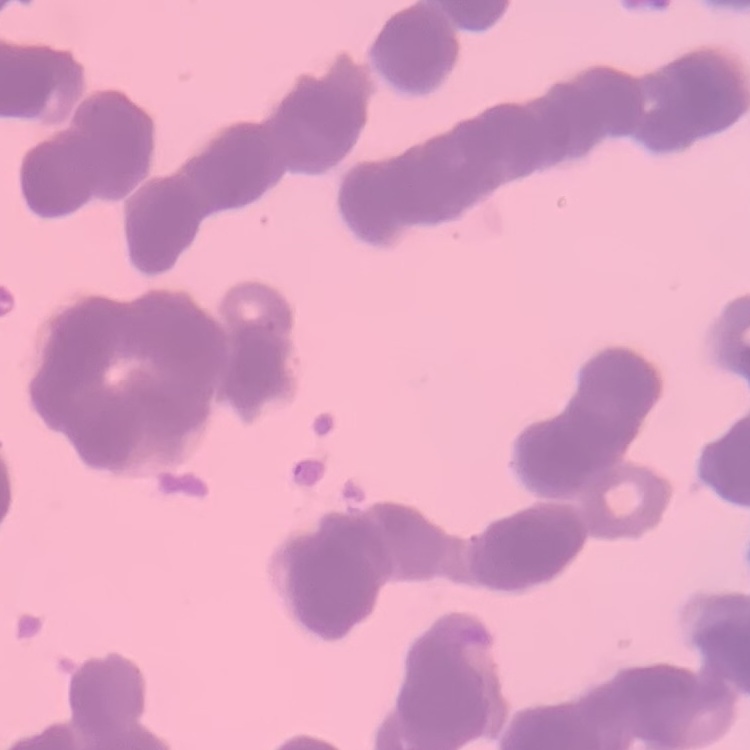

{
  "red_blood_cell_morphology": "rouleaux formation",
  "preparation": "thin peripheral smear",
  "stain": "Field's or Giemsa",
  "image_type": "one tile cut from a larger photomicrograph"
}